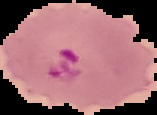

preparation = thin blood film
image size = 157×115 pixels
malaria status = parasitized
image type = cell region segmented out of the field of view; surrounding area masked to black